Outline each Plasmodium falciparum-infected red blood cell.
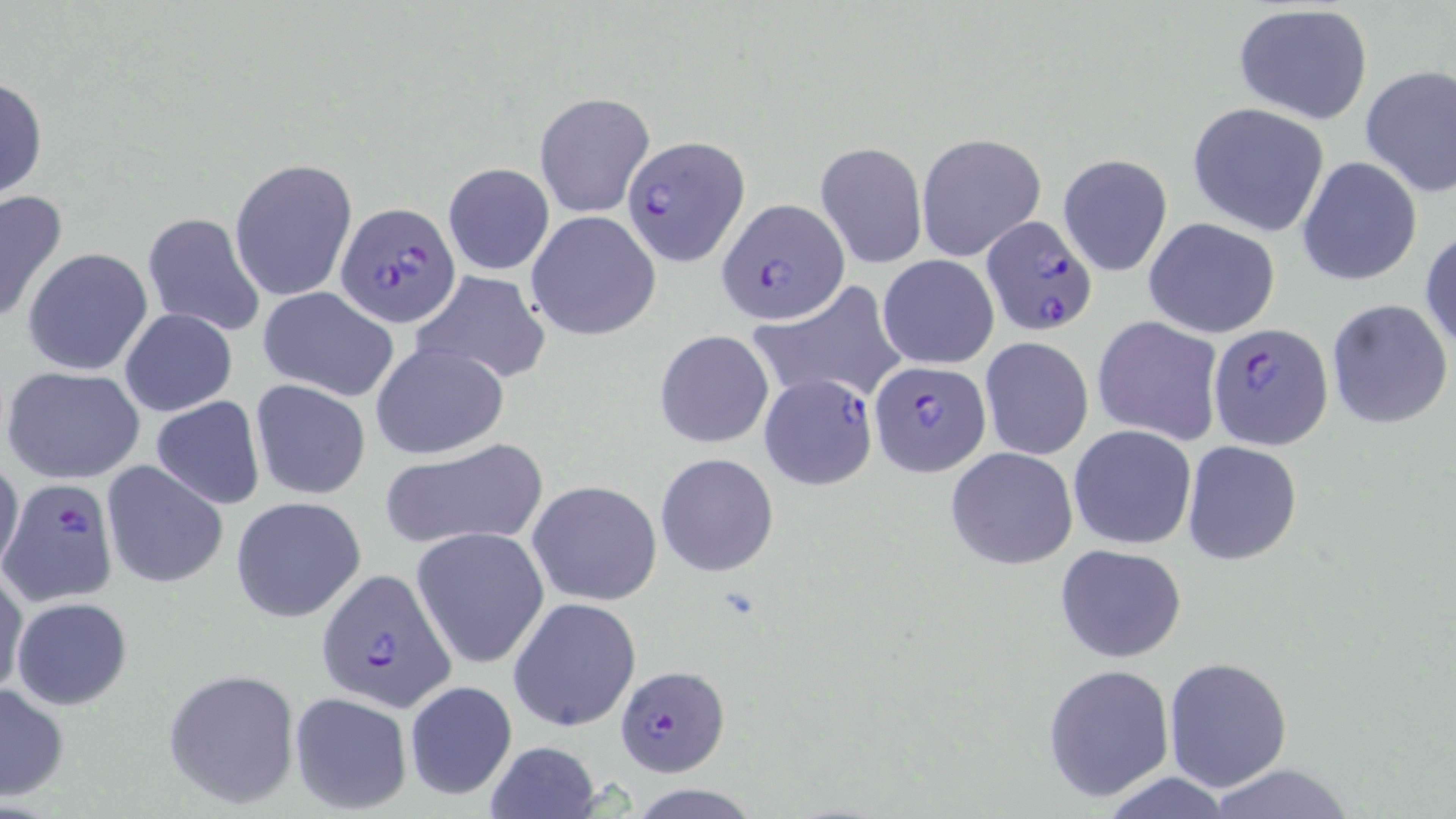

Approximate bounding boxes as (x1, y1, x2, y2) in pixels.
Plasmodium falciparum-infected red blood cells: (621, 136, 747, 267), (717, 197, 849, 323), (336, 200, 461, 326), (979, 214, 1097, 335), (1207, 321, 1333, 448), (869, 361, 989, 477), (757, 374, 876, 488), (2, 480, 118, 607), (316, 569, 455, 710), (614, 665, 729, 777).

Uninfected red blood cell locations: (1231, 5, 1374, 126), (1360, 65, 1456, 197), (0, 74, 48, 202), (534, 91, 655, 218), (1188, 102, 1331, 237), (916, 132, 1047, 264), (815, 140, 928, 269), (1057, 152, 1173, 277), (1297, 157, 1422, 287), (229, 160, 358, 302), (442, 161, 556, 276), (0, 188, 69, 327), (525, 210, 661, 341), (142, 211, 267, 339), (1143, 217, 1281, 338), (1420, 227, 1456, 355), (23, 247, 153, 376), (878, 254, 1000, 369), (410, 271, 552, 385), (749, 281, 906, 407), (257, 287, 401, 402), (1326, 298, 1453, 430), (120, 308, 237, 418), (1092, 317, 1223, 446), (654, 329, 775, 449), (979, 337, 1095, 460), (371, 342, 508, 459), (3, 365, 146, 485), (250, 378, 371, 500), (152, 396, 265, 509), (1069, 424, 1197, 550), (378, 438, 549, 551), (1182, 440, 1302, 566), (945, 446, 1078, 569), (0, 452, 24, 580), (655, 453, 780, 577), (101, 459, 228, 589), (527, 480, 662, 606), (230, 495, 367, 624), (412, 526, 549, 670), (1053, 543, 1187, 663), (0, 562, 27, 698), (508, 596, 642, 734), (12, 597, 132, 710), (1164, 658, 1292, 790), (1042, 663, 1176, 802), (163, 668, 301, 809), (403, 680, 517, 802), (0, 681, 70, 801), (288, 691, 412, 815), (482, 740, 601, 819), (1200, 763, 1363, 818), (1090, 774, 1243, 818). Slide-level diagnosis: Plasmodium falciparum. Image is 1456×819 pixels. Light microscopy. Captured at 1000x magnification. One field of a larger specimen. Thin blood film. May-Grünwald-Giemsa-stained preparation.